Name the cell type shown.
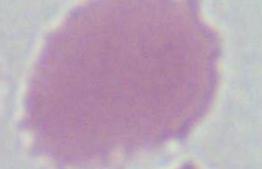
This is an erythrocyte.

magnification = 1000x
modality = micrograph